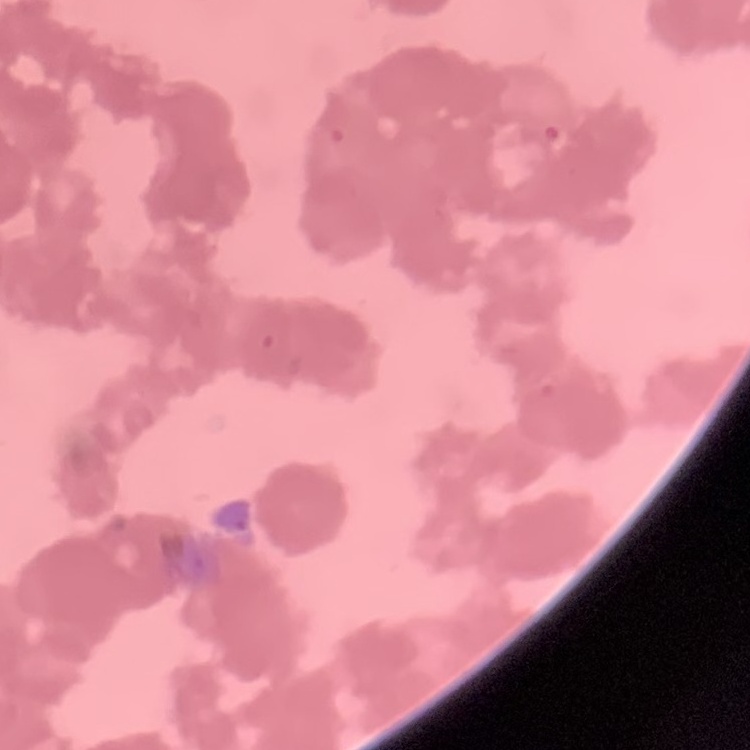

Summary:
  - Red blood cell morphology: rouleaux formation
  - Stain: Field's or Giemsa
  - Preparation: thin blood film
  - Image type: square crop of a larger photomicrograph